Describe the morphology of the erythrocytes.
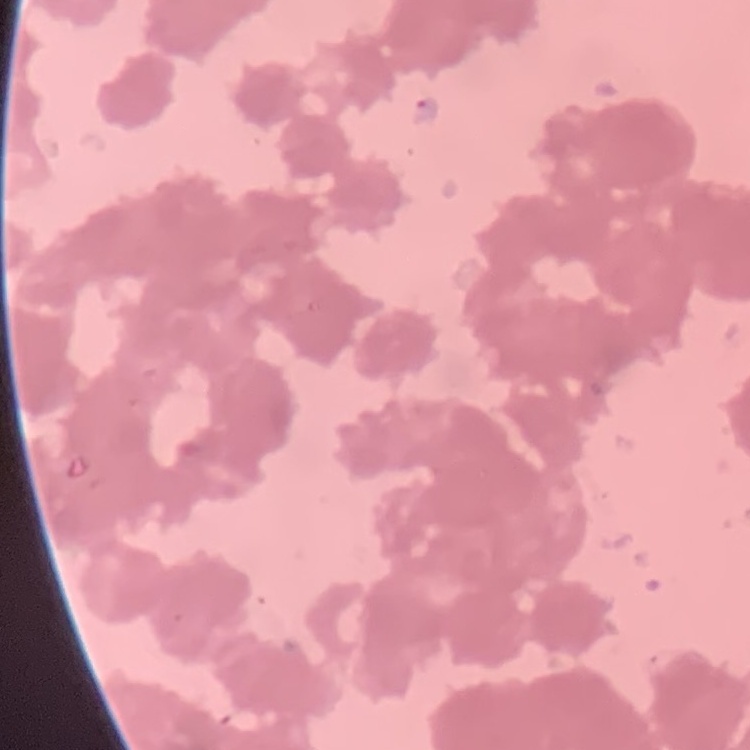

They show rouleaux formation.

Summary:
  - Preparation: thin blood film
  - Stain: Field's or Giemsa
  - Image type: square crop of a larger photomicrograph